Give the extent of all Plasmodium falciparum-infected red blood cells.
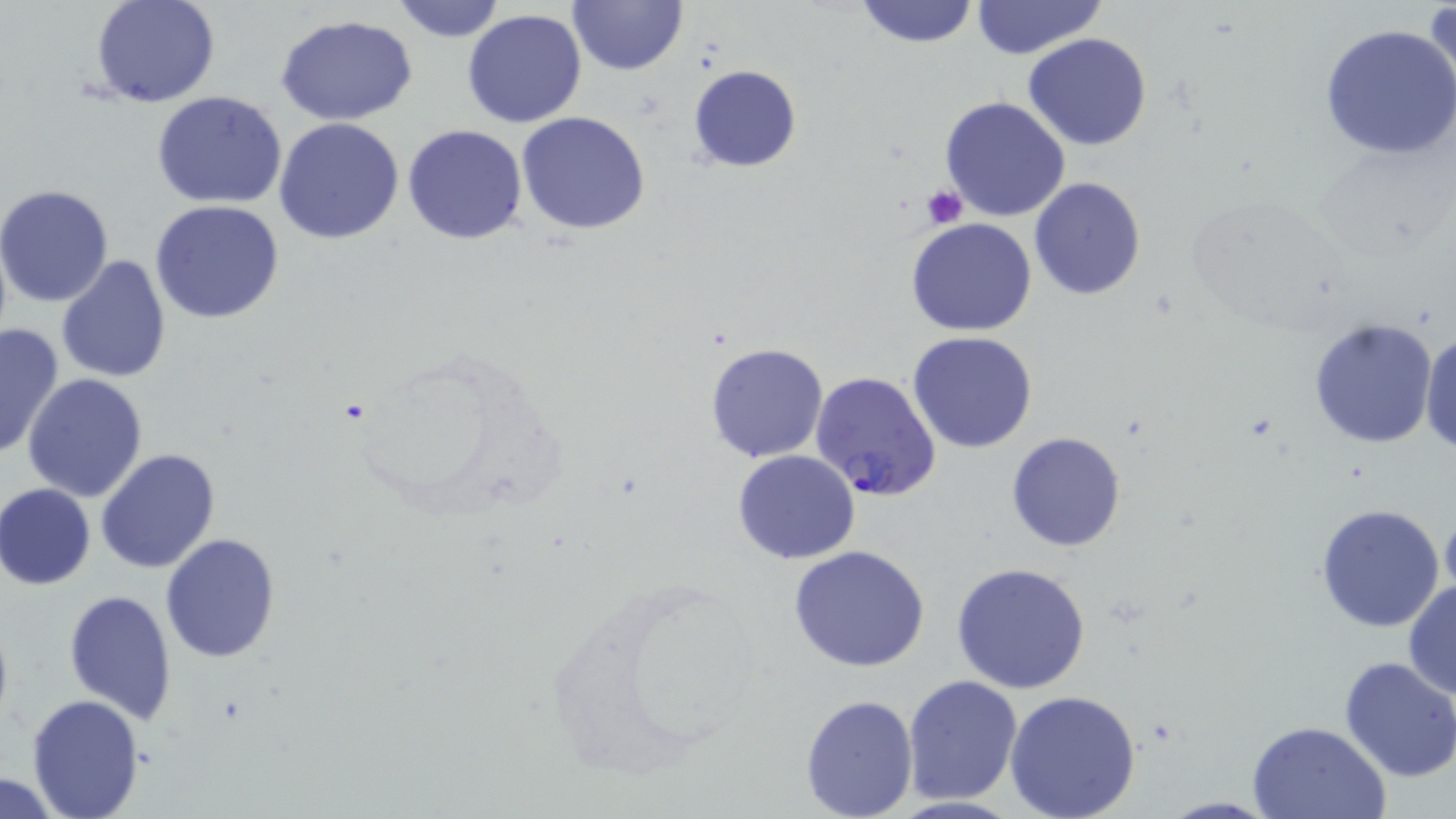

Approximate bounding boxes as (x1,y1)-(x2,y2) corner pairs in pixels.
Plasmodium falciparum-infected red blood cells: (809,370)-(942,501).

Uninfected red blood cell locations: (90,0)-(221,108), (386,0)-(508,43), (565,0)-(689,77), (853,0)-(979,49), (969,1)-(1107,58), (1424,4)-(1455,107), (462,9)-(588,128), (275,13)-(419,125), (1318,23)-(1456,161), (1023,34)-(1152,151), (687,64)-(802,171), (151,91)-(290,209), (939,96)-(1070,223), (515,111)-(651,235), (273,117)-(405,244), (402,123)-(528,245), (1029,177)-(1146,301), (0,184)-(115,308), (149,199)-(285,324), (906,218)-(1038,337), (56,255)-(172,383), (1307,317)-(1440,449), (0,322)-(65,459), (1419,327)-(1456,457), (907,331)-(1039,454), (703,341)-(831,463), (22,373)-(148,503), (1006,431)-(1127,551), (95,448)-(220,574), (732,450)-(860,564), (1,483)-(96,591), (1314,503)-(1446,632), (1440,504)-(1456,605), (160,532)-(281,662), (789,545)-(931,671), (950,561)-(1091,695), (1403,579)-(1456,700), (64,588)-(176,724), (1338,656)-(1456,782), (903,674)-(1022,803), (1004,689)-(1142,819), (26,693)-(145,818), (799,693)-(919,817), (1247,719)-(1393,818), (0,774)-(67,816). Platelet locations: (921,185)-(969,229). Slide-level diagnosis: Plasmodium falciparum. Light microscopy. Captured at 1000x magnification. Thin blood smear. Image is 1456×819 pixels. May-Grünwald-Giemsa-stained preparation. One field of a larger specimen.